Assess this cell for malaria.
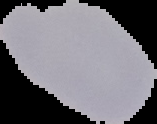
Uninfected.

The area outside the segmented cell region is set to black. Image is 157×124 pixels. From a thin blood film.